Identify the cell.
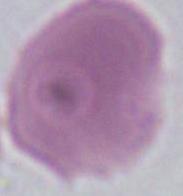

An erythrocyte.

Micrograph. 1000x magnification.